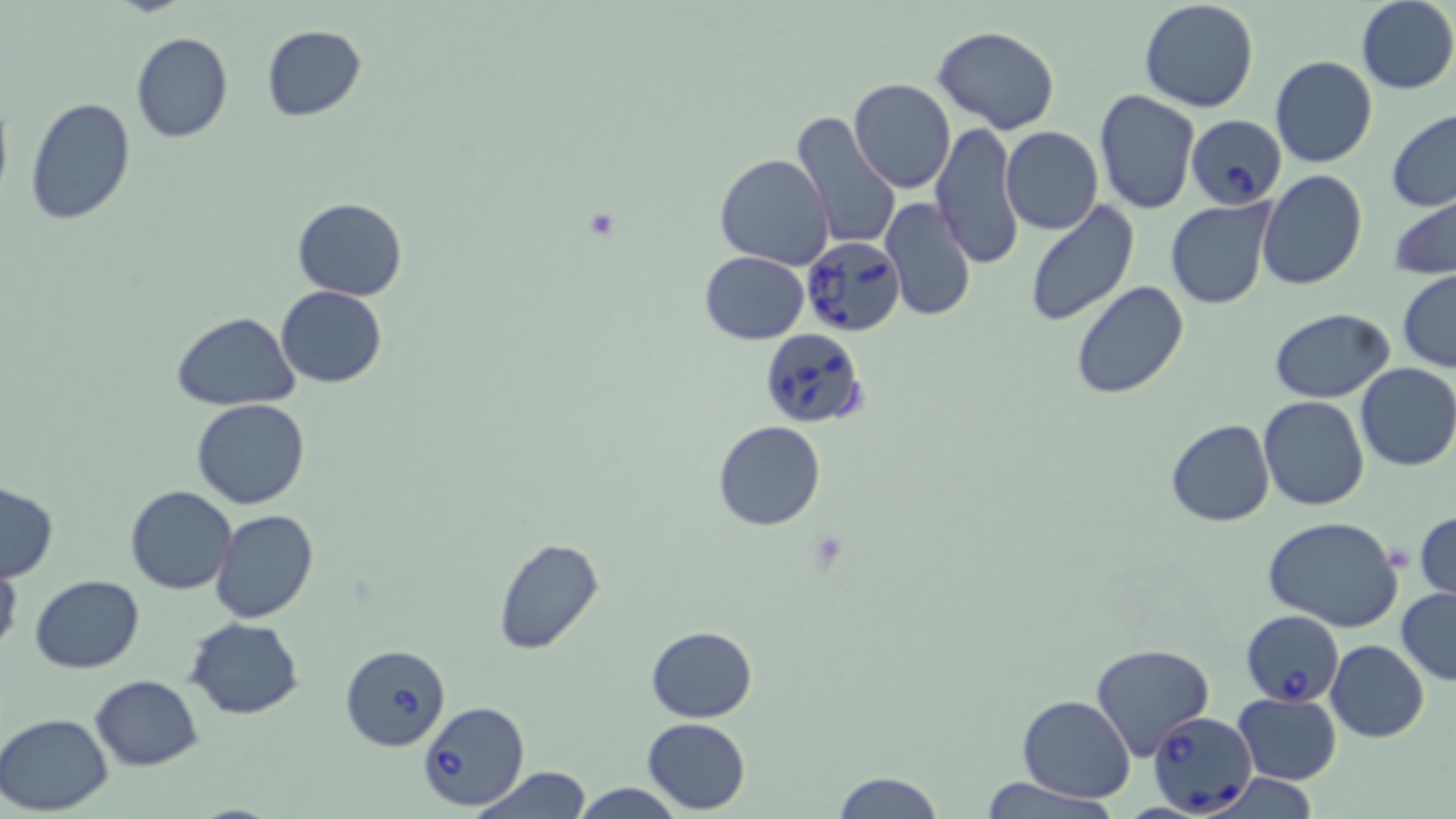

Approximate bounding boxes as named x1/y1/x2/y2 corners in pixels. Babesia divergens-infected red blood cell locations: (x1=1185, y1=114, x2=1287, y2=209), (x1=801, y1=238, x2=907, y2=337), (x1=760, y1=330, x2=867, y2=429), (x1=1241, y1=609, x2=1344, y2=709), (x1=340, y1=644, x2=452, y2=752), (x1=416, y1=701, x2=531, y2=812), (x1=1148, y1=711, x2=1257, y2=817). Uninfected red blood cell locations: (x1=1355, y1=0, x2=1456, y2=93), (x1=1137, y1=1, x2=1260, y2=114), (x1=259, y1=24, x2=368, y2=123), (x1=933, y1=26, x2=1060, y2=132), (x1=129, y1=31, x2=233, y2=143), (x1=1270, y1=55, x2=1377, y2=168), (x1=848, y1=78, x2=957, y2=194), (x1=0, y1=87, x2=13, y2=211), (x1=1093, y1=89, x2=1199, y2=214), (x1=25, y1=97, x2=136, y2=224), (x1=1386, y1=110, x2=1456, y2=213), (x1=790, y1=113, x2=901, y2=252), (x1=931, y1=122, x2=1023, y2=269), (x1=999, y1=126, x2=1103, y2=235), (x1=715, y1=154, x2=835, y2=271), (x1=1256, y1=168, x2=1368, y2=290), (x1=1387, y1=192, x2=1456, y2=279), (x1=292, y1=197, x2=407, y2=302), (x1=880, y1=197, x2=976, y2=323), (x1=1165, y1=198, x2=1278, y2=310), (x1=1023, y1=201, x2=1140, y2=327), (x1=699, y1=251, x2=809, y2=344), (x1=1397, y1=270, x2=1456, y2=373), (x1=1070, y1=280, x2=1191, y2=401), (x1=275, y1=287, x2=387, y2=388), (x1=1269, y1=308, x2=1394, y2=403), (x1=173, y1=312, x2=298, y2=411), (x1=1354, y1=362, x2=1456, y2=470), (x1=1259, y1=396, x2=1370, y2=510), (x1=192, y1=398, x2=309, y2=510), (x1=1165, y1=419, x2=1275, y2=528), (x1=713, y1=421, x2=825, y2=531), (x1=1, y1=482, x2=60, y2=583), (x1=126, y1=485, x2=236, y2=596), (x1=211, y1=508, x2=319, y2=623), (x1=1414, y1=510, x2=1456, y2=603), (x1=1263, y1=516, x2=1404, y2=634), (x1=492, y1=537, x2=604, y2=654), (x1=0, y1=555, x2=21, y2=662), (x1=30, y1=575, x2=145, y2=672), (x1=1396, y1=585, x2=1456, y2=686), (x1=188, y1=618, x2=303, y2=719), (x1=646, y1=625, x2=757, y2=723), (x1=1326, y1=639, x2=1430, y2=743), (x1=1090, y1=644, x2=1215, y2=760), (x1=90, y1=675, x2=203, y2=770), (x1=1233, y1=692, x2=1342, y2=783), (x1=1017, y1=695, x2=1137, y2=803), (x1=0, y1=713, x2=117, y2=815), (x1=642, y1=717, x2=751, y2=814), (x1=471, y1=766, x2=593, y2=818), (x1=831, y1=771, x2=945, y2=819), (x1=975, y1=775, x2=1118, y2=819), (x1=573, y1=781, x2=683, y2=818). Slide-level diagnosis: Babesia divergens. Thin blood film. Light microscopy. Image is 1456×819 pixels. Single field of view. Captured at 1000x magnification. May-Grünwald-Giemsa-stained preparation.